State the blood parasite species.
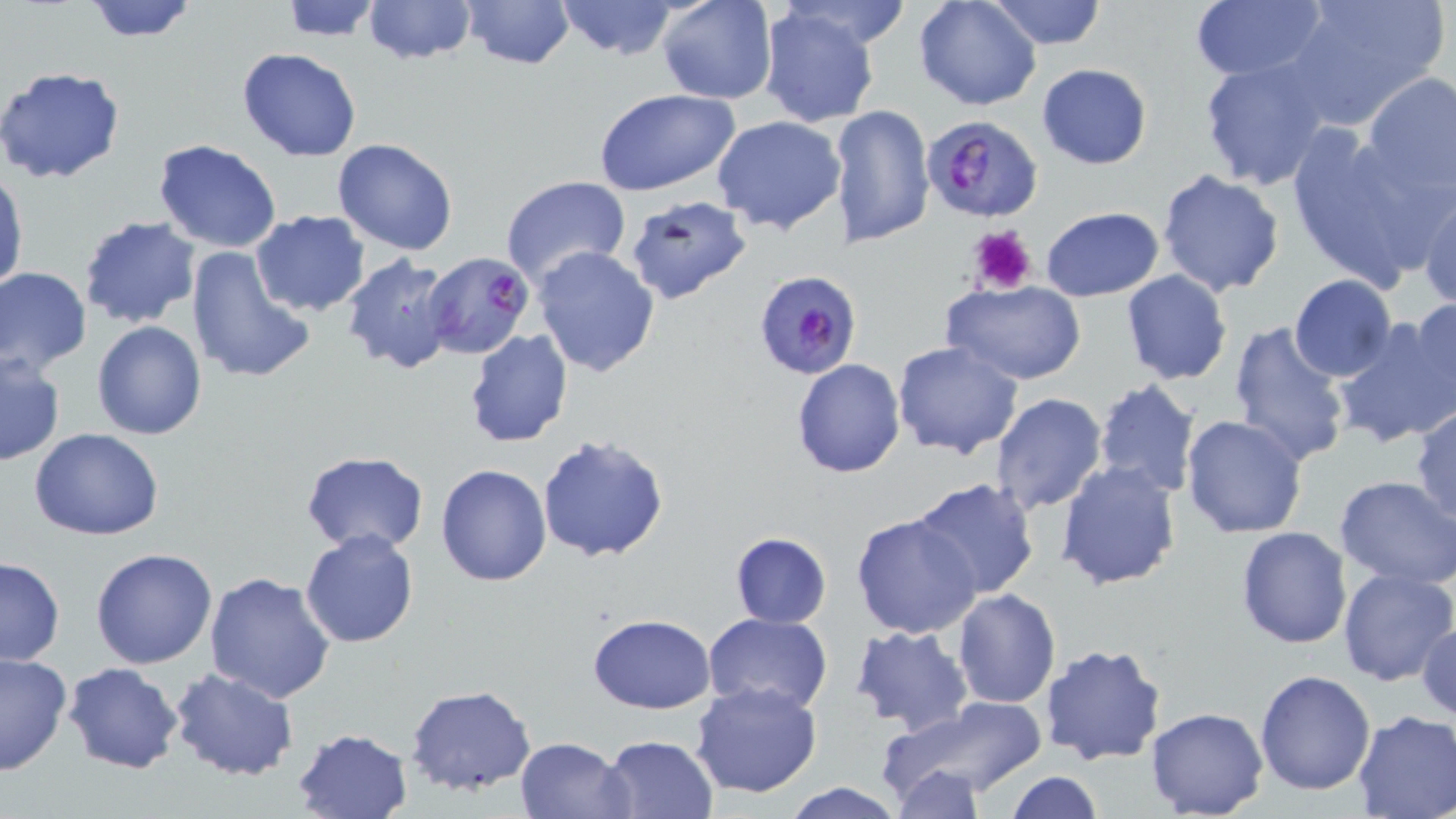
Plasmodium falciparum.

stain = May-Grünwald-Giemsa
magnification = 1000x
image size = 1456×819 pixels
uninfected red blood cell locations = approximate bounding boxes as named x1/y1/x2/y2 corners in pixels: (x1=80, y1=0, x2=200, y2=43), (x1=279, y1=0, x2=387, y2=41), (x1=361, y1=0, x2=477, y2=67), (x1=459, y1=0, x2=576, y2=71), (x1=553, y1=0, x2=683, y2=60), (x1=656, y1=0, x2=779, y2=105), (x1=988, y1=0, x2=1108, y2=50), (x1=1189, y1=0, x2=1327, y2=83), (x1=1284, y1=0, x2=1448, y2=126), (x1=914, y1=1, x2=1041, y2=111), (x1=757, y1=6, x2=882, y2=129), (x1=236, y1=48, x2=363, y2=162), (x1=1199, y1=60, x2=1330, y2=191), (x1=1036, y1=63, x2=1153, y2=170), (x1=0, y1=65, x2=126, y2=184), (x1=1361, y1=71, x2=1455, y2=197), (x1=595, y1=89, x2=739, y2=196), (x1=827, y1=104, x2=935, y2=251), (x1=712, y1=115, x2=847, y2=234), (x1=1285, y1=127, x2=1434, y2=287), (x1=332, y1=139, x2=458, y2=255), (x1=152, y1=140, x2=283, y2=253), (x1=0, y1=169, x2=26, y2=296), (x1=1157, y1=169, x2=1286, y2=298), (x1=500, y1=175, x2=631, y2=288), (x1=1418, y1=192, x2=1455, y2=311), (x1=624, y1=194, x2=750, y2=305), (x1=1041, y1=206, x2=1164, y2=301), (x1=250, y1=210, x2=369, y2=316), (x1=79, y1=215, x2=200, y2=328), (x1=185, y1=245, x2=316, y2=386), (x1=532, y1=246, x2=660, y2=377), (x1=339, y1=252, x2=459, y2=377), (x1=0, y1=267, x2=92, y2=373), (x1=1120, y1=269, x2=1233, y2=385), (x1=1288, y1=275, x2=1396, y2=382), (x1=940, y1=280, x2=1086, y2=386), (x1=1409, y1=297, x2=1455, y2=412), (x1=1331, y1=317, x2=1456, y2=447), (x1=91, y1=319, x2=208, y2=439), (x1=1228, y1=320, x2=1352, y2=466), (x1=464, y1=329, x2=573, y2=447), (x1=892, y1=340, x2=1023, y2=460), (x1=0, y1=353, x2=65, y2=466), (x1=791, y1=357, x2=906, y2=478), (x1=1092, y1=378, x2=1201, y2=499), (x1=1097, y1=391, x2=1299, y2=515), (x1=990, y1=392, x2=1107, y2=515), (x1=1410, y1=405, x2=1456, y2=525), (x1=1182, y1=415, x2=1308, y2=538), (x1=30, y1=427, x2=163, y2=541), (x1=537, y1=432, x2=671, y2=563), (x1=300, y1=450, x2=429, y2=555), (x1=1056, y1=460, x2=1183, y2=591), (x1=435, y1=462, x2=553, y2=585), (x1=1334, y1=474, x2=1456, y2=588), (x1=909, y1=478, x2=1040, y2=603), (x1=850, y1=513, x2=983, y2=640), (x1=1235, y1=526, x2=1353, y2=649), (x1=299, y1=530, x2=419, y2=647), (x1=730, y1=532, x2=832, y2=628), (x1=91, y1=547, x2=217, y2=668), (x1=0, y1=557, x2=65, y2=668), (x1=1336, y1=567, x2=1455, y2=687), (x1=204, y1=570, x2=336, y2=703), (x1=951, y1=589, x2=1061, y2=710), (x1=704, y1=612, x2=834, y2=713), (x1=587, y1=614, x2=716, y2=712), (x1=1416, y1=617, x2=1456, y2=725), (x1=849, y1=625, x2=974, y2=735), (x1=1039, y1=644, x2=1168, y2=766), (x1=0, y1=653, x2=72, y2=776), (x1=62, y1=663, x2=183, y2=774), (x1=170, y1=669, x2=297, y2=781), (x1=1255, y1=670, x2=1376, y2=793), (x1=690, y1=680, x2=822, y2=800), (x1=404, y1=684, x2=539, y2=797), (x1=884, y1=695, x2=1052, y2=802), (x1=1146, y1=706, x2=1269, y2=818), (x1=1351, y1=711, x2=1456, y2=819), (x1=291, y1=727, x2=412, y2=818), (x1=599, y1=733, x2=719, y2=818), (x1=513, y1=735, x2=631, y2=818), (x1=891, y1=766, x2=986, y2=817), (x1=1004, y1=772, x2=1105, y2=818), (x1=779, y1=782, x2=906, y2=819)
field of view = single
modality = light microscopy
preparation = thin blood film
platelet locations = approximate bounding boxes as named x1/y1/x2/y2 corners in pixels: (x1=968, y1=225, x2=1036, y2=295)
Plasmodium falciparum-infected red blood cell locations = approximate bounding boxes as named x1/y1/x2/y2 corners in pixels: (x1=921, y1=113, x2=1044, y2=223), (x1=424, y1=252, x2=533, y2=361), (x1=752, y1=269, x2=861, y2=380)